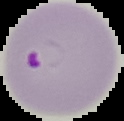

The area outside the segmented cell region is set to black. Image is 124×121 pixels. From a thin blood film. Malaria status: parasitized.